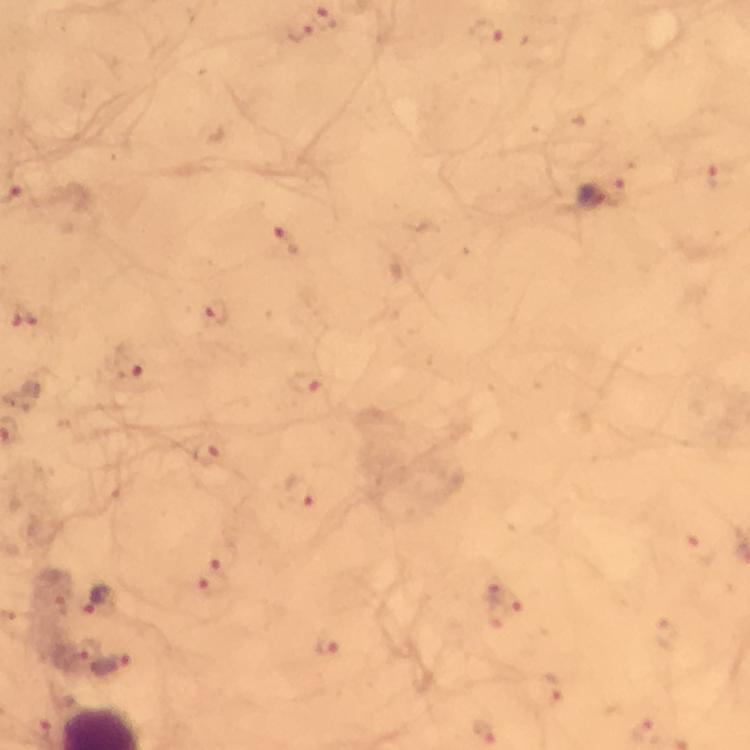

Approximate object centers, in pixels from the top-left corner. Plasmodium parasite locations: (x=328, y=17), (x=301, y=29), (x=484, y=32), (x=723, y=177), (x=622, y=190), (x=591, y=192), (x=287, y=239), (x=218, y=313), (x=25, y=320), (x=129, y=365), (x=308, y=384), (x=208, y=453), (x=301, y=493), (x=705, y=551), (x=225, y=553), (x=214, y=581), (x=100, y=600), (x=504, y=602), (x=667, y=636), (x=329, y=645), (x=83, y=649), (x=111, y=663), (x=551, y=690), (x=486, y=730). Image is 750×750 pixels. Giemsa stain. Thick blood smear. From a diagnostic examination for malaria. Immersion oil applied. Cropped region of a single field of view. 100x magnification. Smartphone photograph taken through a microscope.